Give the extent of all Plasmodium falciparum-infected red blood cells.
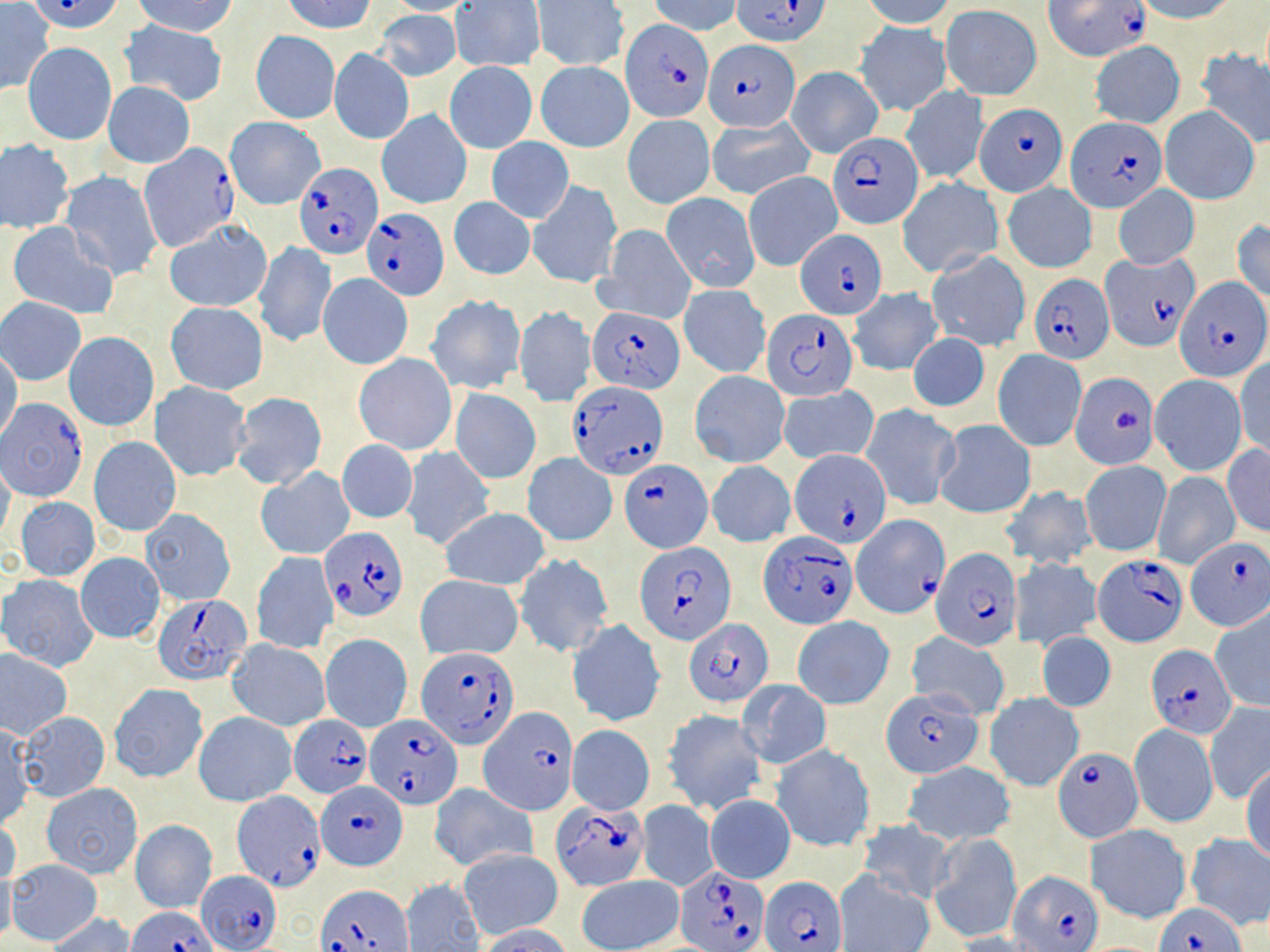

Approximate bounding boxes as (x1, y1, x2, y2) in pixels.
Plasmodium falciparum-infected red blood cells (subset): (29, 0, 126, 34), (733, 0, 832, 47), (1045, 0, 1151, 63), (622, 21, 711, 122), (704, 39, 801, 132), (976, 104, 1066, 196), (1067, 117, 1165, 212), (829, 132, 923, 229), (137, 146, 238, 251), (294, 162, 382, 259), (361, 208, 449, 299), (796, 227, 886, 319), (1099, 253, 1200, 352), (1029, 274, 1115, 362), (1176, 277, 1266, 383), (763, 307, 855, 402), (588, 308, 686, 394), (1072, 371, 1157, 468), (570, 381, 668, 479), (2, 399, 88, 500), (789, 449, 892, 549), (620, 460, 712, 552), (852, 515, 946, 618), (321, 527, 407, 621), (759, 533, 856, 629), (1184, 537, 1270, 631), (638, 541, 735, 643), (931, 545, 1021, 650), (1092, 554, 1189, 647), (153, 594, 254, 686), (684, 619, 773, 705), (1148, 644, 1236, 739), (416, 646, 522, 749), (480, 706, 574, 814), (289, 713, 371, 799), (367, 714, 463, 810), (1054, 747, 1143, 842), (316, 779, 408, 871), (231, 788, 323, 893), (550, 801, 649, 892), (677, 866, 769, 950), (197, 868, 281, 951), (1008, 869, 1102, 951), (763, 875, 848, 952), (316, 884, 412, 952), (1155, 900, 1246, 952), (127, 904, 218, 952).

Summary:
  - Uninfected red blood cell locations (subset): (283, 0, 376, 35), (382, 0, 481, 15), (860, 0, 958, 28), (1130, 0, 1240, 23), (131, 1, 238, 38), (452, 1, 545, 71), (534, 1, 628, 70), (649, 1, 740, 36), (1, 2, 54, 95), (940, 5, 1041, 100), (374, 10, 459, 81), (120, 21, 228, 105), (855, 21, 952, 115), (251, 31, 340, 124), (1090, 41, 1184, 129), (24, 43, 116, 145), (329, 48, 413, 144), (1197, 48, 1270, 147), (444, 61, 537, 153), (535, 61, 635, 152), (787, 67, 882, 158), (104, 83, 194, 168), (900, 86, 989, 185), (1159, 105, 1261, 206), (377, 109, 472, 208), (623, 114, 713, 207), (225, 117, 325, 209), (708, 117, 814, 202), (486, 136, 574, 224), (0, 140, 74, 233), (60, 170, 163, 282), (744, 170, 841, 271), (897, 177, 1005, 278), (528, 178, 621, 287), (1002, 182, 1097, 273), (1114, 184, 1199, 269), (661, 192, 761, 293), (449, 197, 535, 280), (915, 202, 1026, 323), (163, 218, 272, 312), (1232, 219, 1270, 305), (7, 222, 118, 321), (596, 224, 696, 325), (253, 241, 336, 348), (926, 250, 1030, 352), (319, 273, 410, 369), (678, 285, 769, 378), (848, 288, 943, 376), (426, 294, 526, 394), (1, 298, 86, 384), (166, 301, 269, 395), (513, 305, 595, 407), (65, 332, 158, 430), (908, 332, 989, 412), (0, 349, 23, 445), (992, 349, 1086, 450), (354, 353, 457, 455), (1235, 356, 1270, 460), (690, 369, 789, 467), (1148, 374, 1247, 476), (150, 382, 252, 481), (780, 386, 877, 463), (450, 387, 541, 484), (956, 387, 1078, 504), (230, 391, 327, 492), (860, 403, 960, 512), (934, 419, 1035, 519), (89, 436, 181, 537), (338, 440, 418, 523), (1222, 443, 1269, 537), (401, 446, 495, 551), (946, 451, 1070, 551), (523, 454, 617, 546), (0, 459, 16, 545), (707, 461, 795, 547), (1080, 461, 1171, 556), (256, 468, 355, 559), (1152, 471, 1239, 569), (999, 485, 1097, 570), (15, 497, 101, 580), (439, 507, 551, 590), (141, 509, 233, 605), (251, 551, 337, 655), (75, 552, 165, 644), (513, 554, 613, 656), (1011, 558, 1101, 650), (1, 574, 99, 671), (415, 576, 523, 661), (1210, 606, 1270, 713), (793, 616, 895, 709), (569, 620, 665, 725), (906, 631, 1010, 719), (1037, 631, 1115, 712), (320, 634, 412, 733), (226, 640, 330, 732), (1, 651, 71, 738), (737, 679, 831, 769), (109, 683, 208, 782), (985, 693, 1084, 792), (1204, 702, 1270, 806), (662, 709, 768, 815), (19, 712, 110, 802), (194, 712, 296, 807), (567, 724, 655, 815), (1129, 724, 1219, 828), (1, 725, 33, 827), (771, 745, 873, 851), (903, 761, 1015, 845), (1242, 764, 1270, 865), (42, 783, 142, 877), (429, 783, 536, 871), (704, 794, 795, 884), (637, 800, 718, 891), (0, 814, 21, 891), (856, 818, 956, 903), (130, 819, 217, 912), (1084, 824, 1191, 925), (1184, 832, 1270, 930), (929, 833, 1021, 942), (458, 848, 562, 941), (7, 859, 102, 944), (0, 868, 17, 947), (834, 868, 934, 952), (575, 875, 683, 952), (401, 879, 485, 951), (46, 912, 136, 952), (475, 924, 574, 952)
  - Slide-level diagnosis: Plasmodium falciparum
  - Field of view: single
  - Preparation: thin blood film
  - Modality: light microscopy
  - Magnification: 1000x
  - Stain: May-Grünwald-Giemsa
  - Image size: 1270×952 pixels